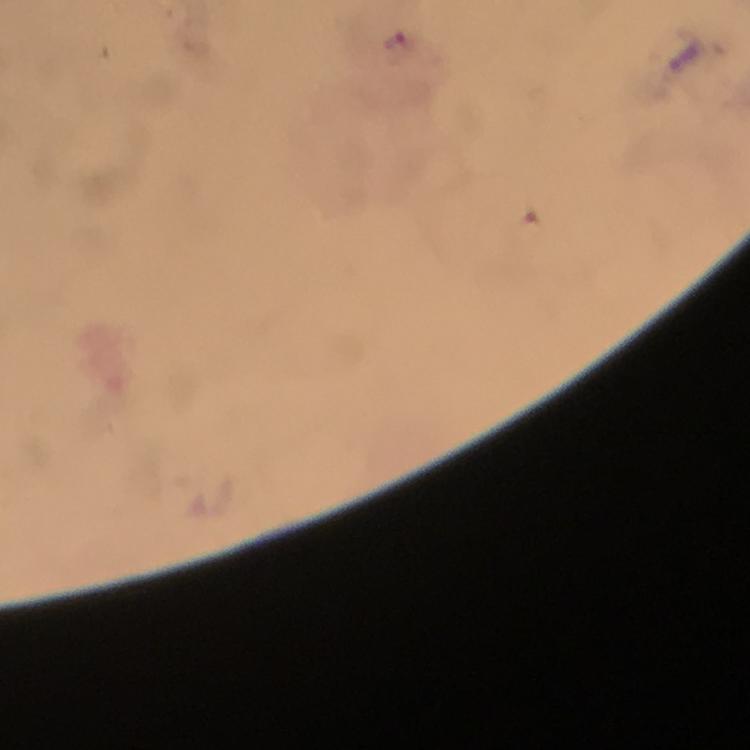
Approximate centers as {x, y} in pixels. Plasmodium parasite locations: {399, 47}. A crop from one field of view. Immersion oil was used. Thick blood film. Giemsa-stained preparation. Image is 750×750 pixels. 100x magnification. Smartphone photograph taken through a microscope. From a malaria diagnostic workup.